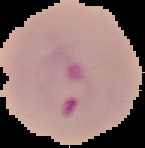
Summary:
  - Image type: segmented cell region on a black background
  - Preparation: thin blood film
  - Result: Plasmodium parasites detected
  - Image size: 145×148 pixels